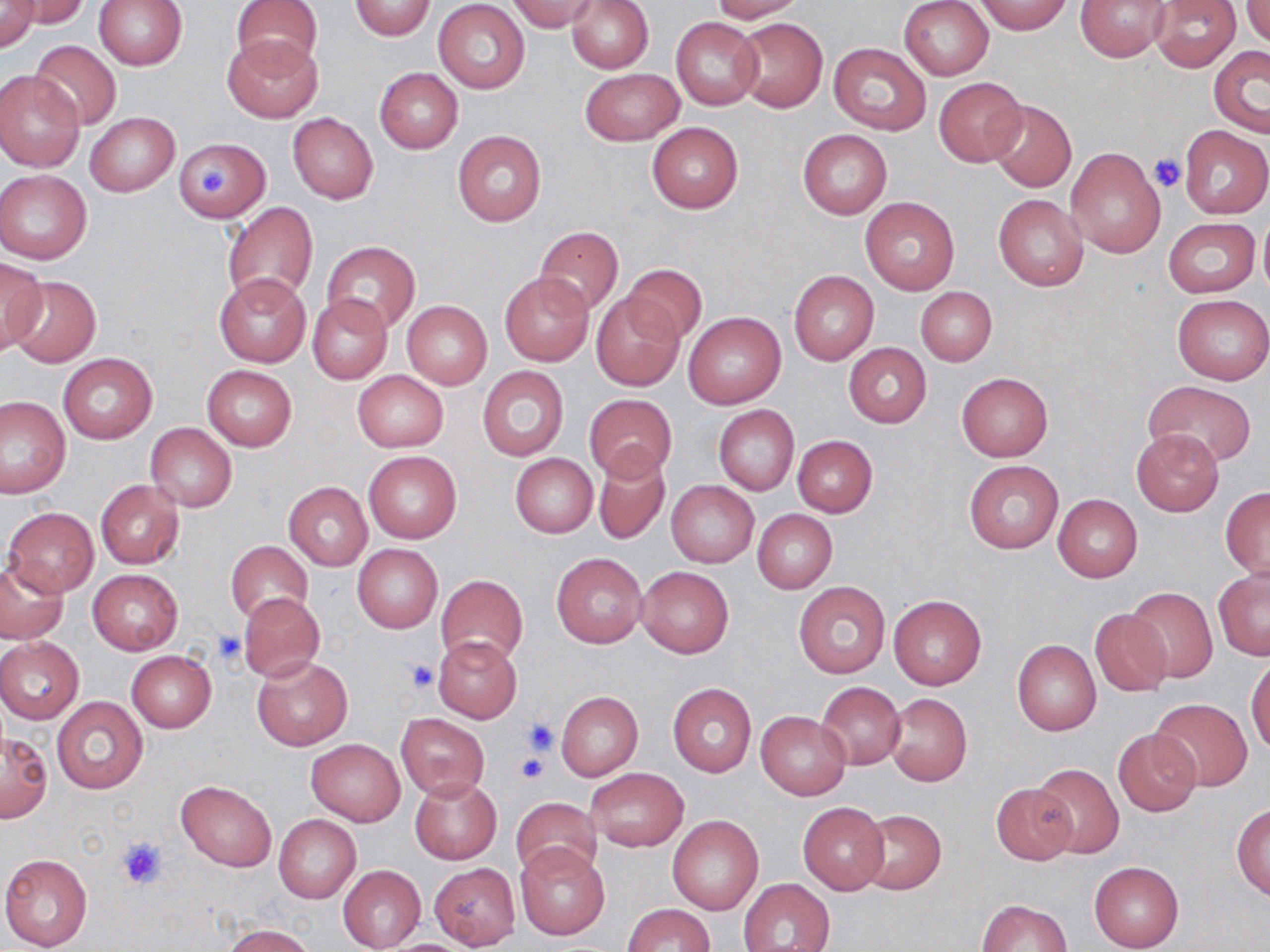

Summary:
  - Coordinate format: approximate bounding boxes as (x1, y1, x2, y2) in pixels
  - Uninfected red blood cell locations: (9, 0, 89, 28), (94, 0, 187, 69), (231, 0, 322, 75), (348, 0, 436, 41), (507, 0, 600, 33), (566, 0, 653, 73), (709, 0, 806, 22), (900, 0, 994, 80), (1076, 0, 1173, 62), (1149, 0, 1241, 72), (1241, 0, 1270, 46), (974, 1, 1074, 34), (0, 2, 40, 53), (433, 2, 530, 93), (733, 15, 827, 112), (671, 17, 763, 109), (223, 36, 323, 123), (28, 38, 121, 131), (829, 42, 932, 135), (1209, 45, 1270, 136), (374, 67, 463, 154), (580, 68, 684, 146), (0, 70, 84, 171), (934, 77, 1027, 167), (987, 99, 1076, 193), (86, 113, 178, 196), (288, 113, 378, 203), (646, 122, 744, 213), (1179, 126, 1270, 218), (452, 130, 547, 226), (798, 130, 891, 219), (172, 136, 273, 224), (1065, 148, 1165, 257), (1, 170, 92, 263), (993, 193, 1089, 291), (860, 197, 960, 294), (222, 202, 319, 306), (1257, 209, 1270, 299), (1163, 217, 1259, 297), (534, 226, 624, 316), (322, 241, 421, 333), (0, 256, 45, 355), (620, 264, 707, 348), (498, 271, 593, 367), (789, 271, 879, 366), (213, 272, 312, 368), (6, 275, 102, 369), (916, 286, 997, 366), (308, 294, 392, 384), (1172, 294, 1269, 384), (593, 295, 683, 390), (402, 300, 492, 389), (683, 310, 786, 409), (844, 342, 932, 428), (58, 354, 157, 444), (202, 365, 297, 451), (477, 366, 568, 459), (352, 370, 448, 452), (956, 372, 1052, 460), (1142, 380, 1256, 467), (583, 394, 678, 483), (1, 395, 70, 496), (714, 404, 799, 495), (144, 422, 237, 513), (1132, 429, 1224, 515), (792, 435, 877, 516), (363, 451, 462, 543), (592, 451, 671, 544), (510, 453, 598, 538), (963, 460, 1063, 553), (96, 480, 185, 569), (666, 480, 759, 568), (284, 482, 372, 570), (1220, 487, 1270, 581), (1053, 494, 1143, 582), (4, 506, 100, 598), (752, 510, 837, 594), (225, 540, 314, 625), (353, 544, 442, 632), (552, 553, 647, 647), (0, 560, 68, 643), (637, 565, 733, 659), (1213, 568, 1270, 660), (87, 569, 183, 654), (435, 574, 527, 666), (793, 581, 890, 678), (1128, 587, 1219, 684), (239, 592, 325, 683), (889, 594, 987, 690), (1090, 608, 1174, 696), (432, 636, 522, 722), (0, 638, 84, 724), (1012, 640, 1100, 735), (126, 650, 216, 733), (252, 656, 352, 750), (1246, 659, 1270, 754), (817, 682, 905, 770), (667, 683, 756, 776), (556, 691, 643, 780), (883, 693, 972, 787), (52, 697, 147, 793), (1150, 699, 1253, 790), (755, 710, 850, 799), (396, 714, 488, 799), (1113, 729, 1202, 816), (2, 732, 53, 823), (306, 739, 405, 826), (1031, 764, 1123, 859), (585, 768, 689, 851), (409, 776, 501, 864), (176, 780, 276, 872), (991, 782, 1080, 866), (511, 797, 602, 881), (798, 802, 889, 895), (1232, 803, 1270, 899), (858, 809, 945, 894), (273, 814, 361, 904), (668, 814, 764, 915), (514, 842, 611, 941), (0, 852, 93, 950), (1089, 861, 1185, 952), (429, 864, 520, 948), (338, 865, 425, 950), (740, 878, 835, 950), (977, 899, 1072, 952), (623, 903, 713, 951), (223, 924, 314, 952)
  - Platelet locations: (1149, 153, 1186, 193), (196, 164, 229, 198), (212, 630, 246, 666), (405, 661, 440, 693), (522, 719, 559, 755), (515, 753, 549, 783), (116, 835, 170, 892)
  - Slide-level diagnosis: negative for blood parasites
  - Field of view: single
  - Image size: 1270×952 pixels
  - Stain: May-Grünwald-Giemsa
  - Preparation: thin blood smear
  - Modality: optical microscopy
  - Magnification: 1000x